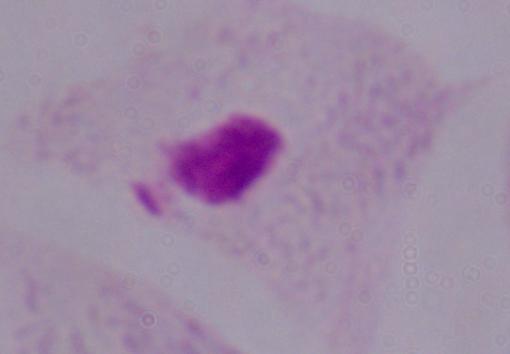
Summary:
  - Identification: trichomonad
  - Magnification: 1000x
  - Modality: micrograph